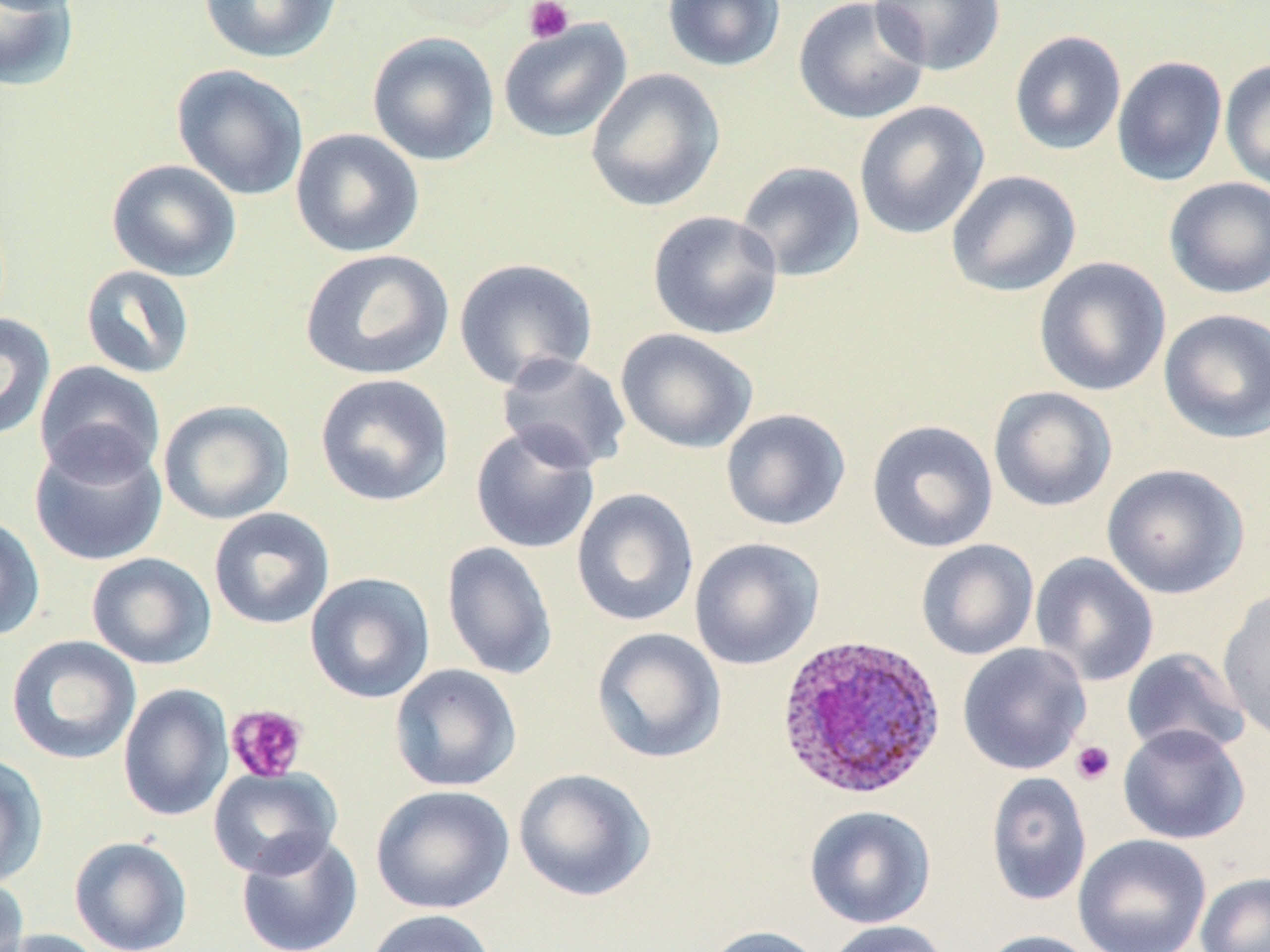
Summary:
  - Coordinate format: approximate bounding boxes as named x1/y1/x2/y2 corners in pixels
  - Uninfected red blood cell locations: (x1=197, y1=0, x2=343, y2=64), (x1=662, y1=0, x2=786, y2=72), (x1=792, y1=0, x2=931, y2=126), (x1=868, y1=0, x2=1007, y2=76), (x1=0, y1=1, x2=81, y2=92), (x1=497, y1=19, x2=632, y2=143), (x1=1008, y1=30, x2=1127, y2=156), (x1=367, y1=32, x2=500, y2=166), (x1=1111, y1=55, x2=1228, y2=186), (x1=1220, y1=59, x2=1270, y2=194), (x1=171, y1=64, x2=310, y2=202), (x1=584, y1=67, x2=726, y2=212), (x1=853, y1=101, x2=990, y2=240), (x1=290, y1=128, x2=425, y2=258), (x1=106, y1=159, x2=242, y2=282), (x1=735, y1=160, x2=866, y2=282), (x1=945, y1=169, x2=1082, y2=298), (x1=1163, y1=176, x2=1270, y2=299), (x1=647, y1=210, x2=784, y2=341), (x1=300, y1=248, x2=454, y2=381), (x1=1033, y1=256, x2=1171, y2=397), (x1=453, y1=257, x2=598, y2=390), (x1=80, y1=264, x2=196, y2=379), (x1=1157, y1=308, x2=1270, y2=444), (x1=0, y1=313, x2=55, y2=441), (x1=615, y1=328, x2=758, y2=454), (x1=495, y1=352, x2=632, y2=473), (x1=33, y1=360, x2=166, y2=484), (x1=314, y1=373, x2=454, y2=507), (x1=988, y1=386, x2=1118, y2=512), (x1=157, y1=399, x2=295, y2=525), (x1=720, y1=407, x2=852, y2=531), (x1=866, y1=419, x2=999, y2=553), (x1=470, y1=424, x2=601, y2=554), (x1=29, y1=434, x2=167, y2=567), (x1=1101, y1=463, x2=1249, y2=599), (x1=571, y1=488, x2=700, y2=628), (x1=208, y1=507, x2=335, y2=630), (x1=0, y1=514, x2=46, y2=642), (x1=689, y1=537, x2=825, y2=670), (x1=916, y1=539, x2=1039, y2=660), (x1=441, y1=541, x2=558, y2=681), (x1=1029, y1=551, x2=1159, y2=687), (x1=86, y1=552, x2=217, y2=670), (x1=305, y1=572, x2=435, y2=704), (x1=1217, y1=586, x2=1270, y2=743), (x1=591, y1=627, x2=727, y2=764), (x1=5, y1=635, x2=141, y2=765), (x1=957, y1=643, x2=1092, y2=775), (x1=1121, y1=647, x2=1251, y2=759), (x1=389, y1=663, x2=522, y2=792), (x1=118, y1=683, x2=234, y2=822), (x1=1117, y1=724, x2=1250, y2=845), (x1=0, y1=753, x2=49, y2=888), (x1=208, y1=766, x2=342, y2=878), (x1=513, y1=767, x2=656, y2=902), (x1=985, y1=771, x2=1093, y2=906), (x1=370, y1=785, x2=515, y2=915), (x1=804, y1=805, x2=936, y2=929), (x1=236, y1=831, x2=363, y2=952), (x1=1073, y1=834, x2=1212, y2=952), (x1=69, y1=835, x2=193, y2=952), (x1=1195, y1=872, x2=1270, y2=952), (x1=0, y1=874, x2=30, y2=952), (x1=363, y1=909, x2=498, y2=952), (x1=823, y1=920, x2=951, y2=952), (x1=702, y1=925, x2=824, y2=952), (x1=2, y1=928, x2=111, y2=952), (x1=978, y1=930, x2=1102, y2=952)
  - Plasmodium ovale-infected red blood cell locations: (x1=775, y1=633, x2=946, y2=801)
  - Platelet locations: (x1=523, y1=0, x2=575, y2=44), (x1=226, y1=704, x2=309, y2=783), (x1=1071, y1=740, x2=1115, y2=785)
  - Slide-level diagnosis: Plasmodium ovale
  - Image size: 1270×952 pixels
  - Stain: May-Grünwald-Giemsa
  - Preparation: thin blood film
  - Magnification: 1000x
  - Modality: light microscopy
  - Field of view: single